Classify this cell by malaria status.
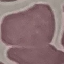
Uninfected.

{
  "capture": "smartphone through the microscope eyepiece",
  "stain": "Giemsa",
  "image_type": "automatically extracted cell patch, resized to 64 × 64 pixels",
  "preparation": "thin smear"
}